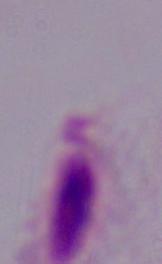

1000x magnification. A trichomonad is seen. Photomicrograph.